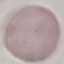

malaria status = uninfected
stain = Giemsa
image type = automatically extracted cell patch, resized to 64 × 64 pixels
capture = smartphone through the microscope eyepiece
preparation = thin blood film